Assess the morphology of the erythrocytes.
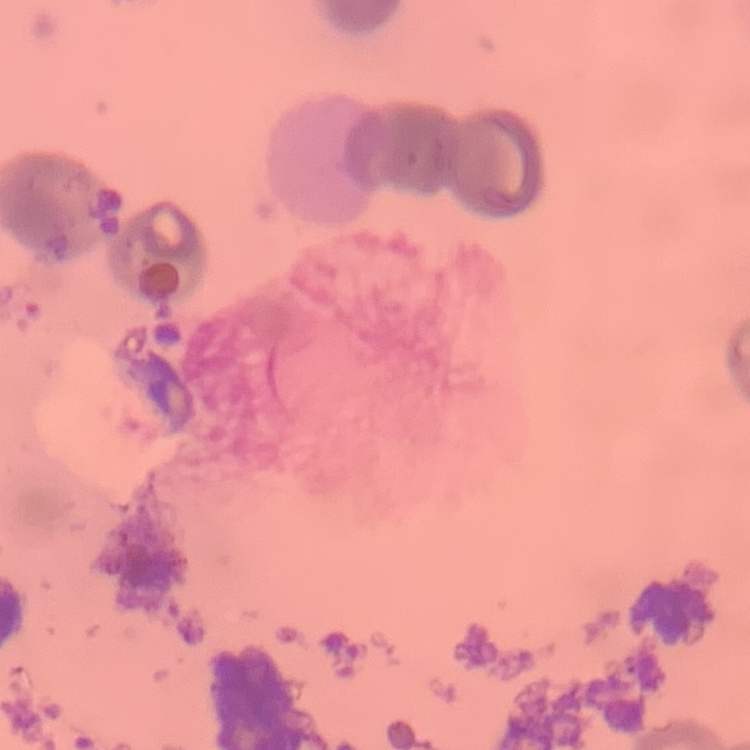

Rouleaux formation.

stain = Field's or Giemsa
preparation = thin peripheral smear
image type = one tile cut from a larger photomicrograph